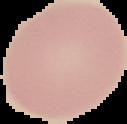 Image is 127×124 pixels. From a thin blood smear. Segmented cell region on a black background. Malaria status: uninfected.